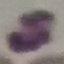
result = no malaria parasites seen
capture = smartphone through the microscope eyepiece
preparation = thin blood film
image type = automatically extracted cell patch, resized to 64 × 64 pixels
stain = Giemsa